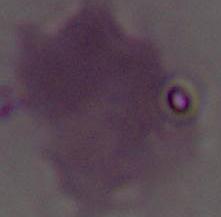
Summary:
  - Identification: red blood cell
  - Modality: micrograph
  - Magnification: 1000x